Describe the morphology of the erythrocytes.
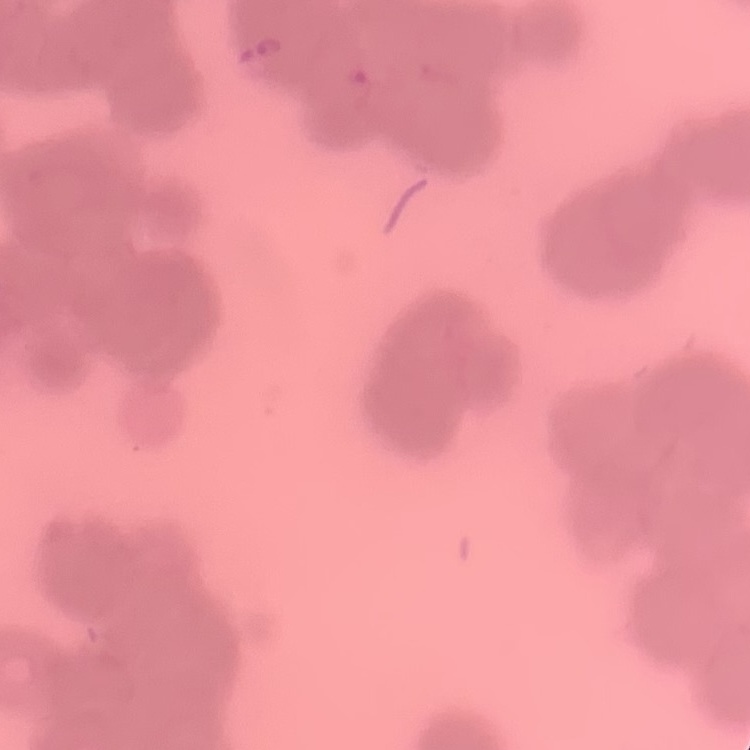
Rouleaux formation.

Stained with either Field's or Giemsa. One tile cut from a larger photomicrograph. Thin blood smear.